State the blood parasite species.
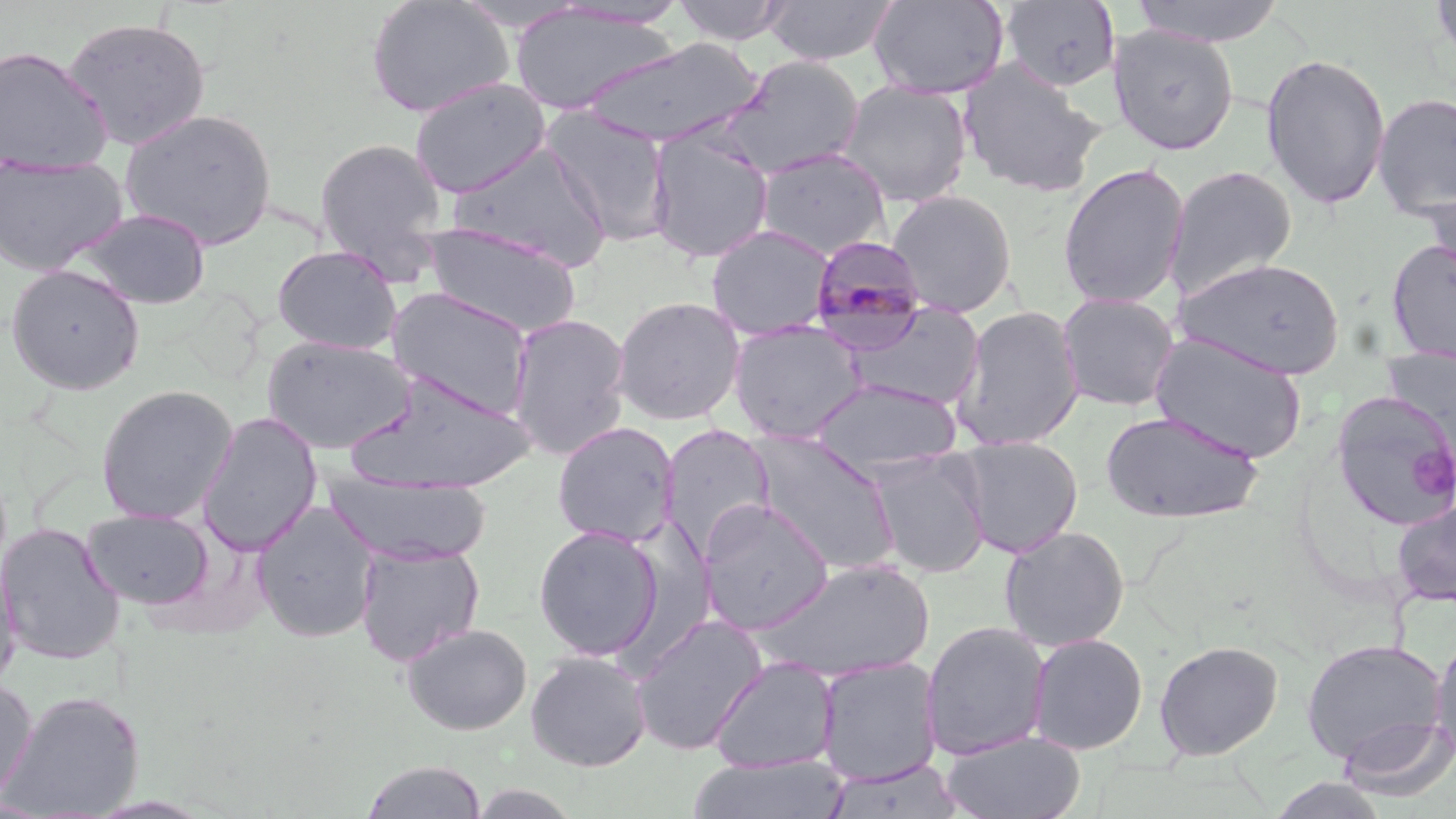

Plasmodium malariae.

Approximate bounding boxes as (x1,y1)-(x2,y2) corner pairs in pixels. Platelet locations: (1411,446)-(1455,495). Plasmodium malariae-infected red blood cell locations: (807,234)-(930,350). Uninfected red blood cell locations: (365,0)-(514,118), (672,0)-(791,46), (761,0)-(899,66), (868,0)-(1009,100), (999,0)-(1121,93), (1129,0)-(1287,47), (1430,0)-(1456,70), (550,2)-(693,29), (508,5)-(679,115), (61,16)-(212,151), (1107,25)-(1239,155), (584,38)-(763,148), (0,45)-(113,174), (1261,52)-(1392,210), (718,55)-(865,179), (957,58)-(1106,199), (409,77)-(552,198), (839,81)-(973,207), (1372,92)-(1456,219), (119,107)-(278,250), (541,107)-(675,246), (646,128)-(774,264), (313,137)-(448,275), (450,143)-(612,270), (754,147)-(891,259), (0,155)-(129,276), (1056,162)-(1190,309), (1165,163)-(1298,300), (1418,184)-(1456,288), (885,189)-(1018,317), (73,207)-(212,311), (421,221)-(582,338), (705,224)-(836,340), (1385,238)-(1456,364), (272,244)-(403,354), (1176,257)-(1346,379), (4,264)-(146,395), (385,286)-(536,419), (1056,292)-(1180,412), (611,296)-(746,425), (844,302)-(985,411), (952,304)-(1085,451), (507,312)-(632,461), (728,321)-(867,444), (1149,331)-(1308,464), (262,335)-(417,454), (344,370)-(537,495), (809,378)-(963,474), (839,381)-(976,547), (95,384)-(238,525), (1330,391)-(1456,531), (1100,410)-(1263,524), (196,412)-(323,555), (551,421)-(680,547), (659,423)-(776,558), (749,432)-(899,574), (955,436)-(1083,558), (868,450)-(991,578), (324,471)-(493,566), (1390,498)-(1456,606), (698,499)-(835,635), (252,502)-(380,643), (81,508)-(215,609), (0,522)-(125,665), (532,524)-(664,662), (999,525)-(1130,651), (355,542)-(485,666), (0,547)-(22,694), (755,558)-(935,683), (630,614)-(767,756), (920,620)-(1051,760), (401,622)-(533,735), (1430,631)-(1456,765), (1027,633)-(1148,755), (1301,637)-(1449,768), (1154,640)-(1283,761), (525,651)-(652,771), (710,656)-(839,774), (816,657)-(943,785), (0,677)-(38,811), (2,689)-(144,818), (1337,714)-(1456,801), (941,731)-(1086,819), (687,754)-(849,819), (823,758)-(966,819), (359,760)-(489,818), (1266,775)-(1392,819). Single field of view. Thin blood smear. Image is 1456×819 pixels. May-Grünwald-Giemsa stain. Captured at 1000x magnification. Optical microscopy.